Assess this cell for malaria.
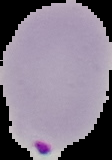

Parasitized.

image type = cell region segmented out of the field of view; surrounding area masked to black
preparation = thin blood smear
image size = 112×160 pixels